Locate every blood parasite and identify its species.
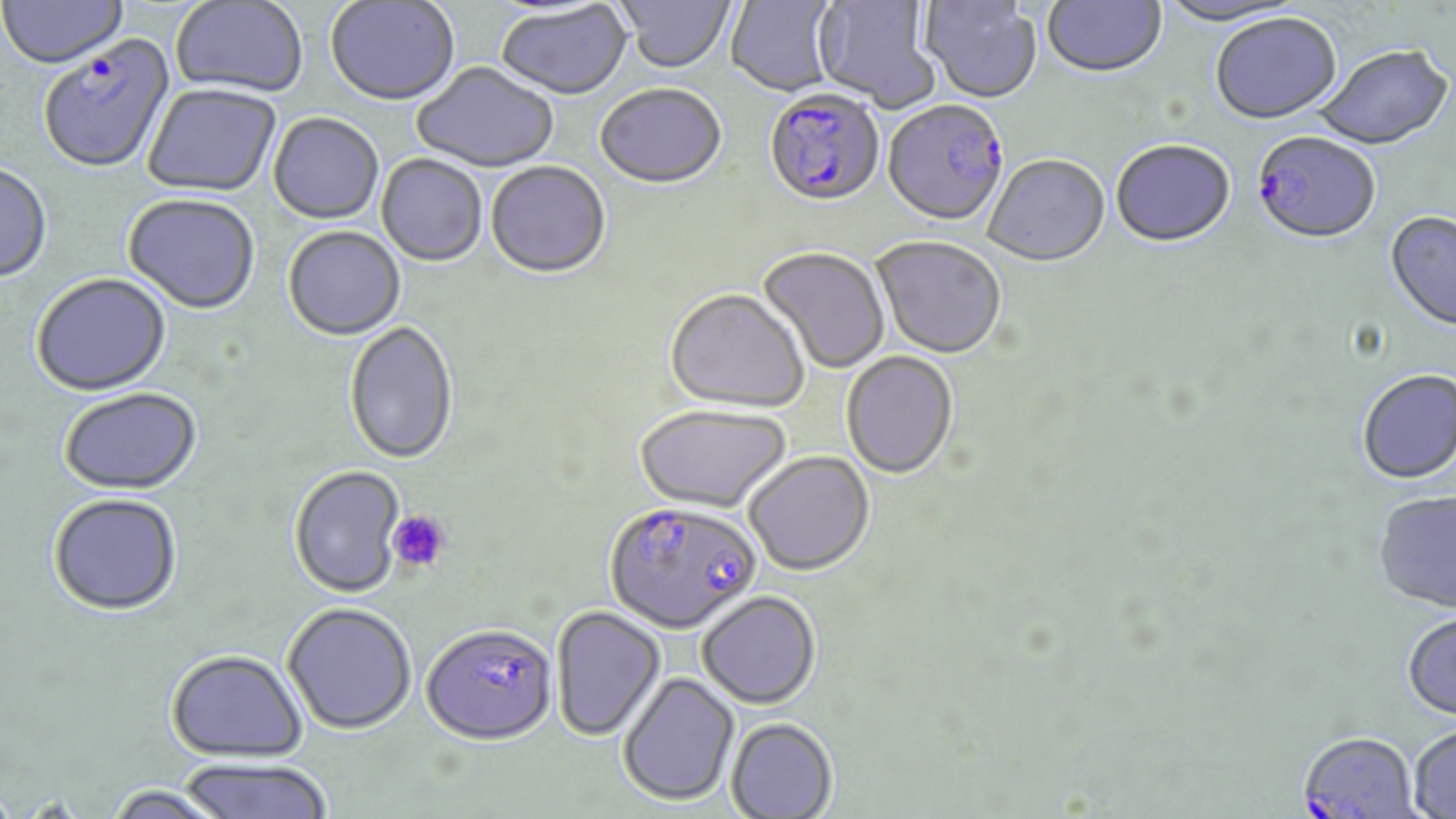

Approximate bounding boxes as (x1,y1)-(x2,y2) corner pairs in pixels.
Plasmodium falciparum-infected red blood cells: (39,39)-(175,175), (763,92)-(886,212), (882,102)-(1010,229), (1252,134)-(1380,247), (605,500)-(762,634), (420,622)-(556,743), (1297,732)-(1420,819).
No Plasmodium ovale, Plasmodium malariae, Plasmodium vivax, Babesia divergens, or Trypanosoma brucei observed.

Platelet locations: (387,510)-(450,573). Uninfected red blood cell locations: (0,0)-(128,71), (171,0)-(308,98), (326,0)-(459,107), (617,0)-(735,75), (726,0)-(839,99), (812,0)-(940,112), (1042,0)-(1168,81), (920,1)-(1043,106), (1158,1)-(1309,29), (496,3)-(633,102), (1210,15)-(1343,128), (1314,47)-(1453,153), (412,63)-(559,174), (144,85)-(281,198), (595,86)-(726,191), (268,114)-(383,225), (1111,142)-(1235,250), (376,155)-(487,268), (984,156)-(1110,269), (486,163)-(610,280), (0,164)-(52,285), (123,195)-(260,315), (1384,212)-(1456,336), (283,227)-(405,341), (871,238)-(1006,361), (758,248)-(890,374), (31,275)-(171,398), (665,291)-(808,415), (344,321)-(458,466), (841,352)-(958,481), (1357,371)-(1456,487), (59,389)-(202,496), (634,406)-(792,514), (744,452)-(875,576), (288,465)-(406,597), (48,493)-(182,616), (1373,493)-(1456,616), (697,590)-(821,708), (282,601)-(416,733), (551,605)-(665,740), (1402,614)-(1456,724), (166,649)-(307,761), (618,671)-(740,806), (726,717)-(838,819), (1408,725)-(1456,818), (176,758)-(333,819), (103,784)-(233,819). Slide-level diagnosis: Plasmodium falciparum. Optical microscopy. One field of a larger specimen. May-Grünwald-Giemsa stain. Image is 1456×819 pixels. Thin blood film. 1000x magnification.